Assess this cell for malaria.
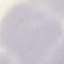
It is uninfected.

Summary:
  - Stain: Giemsa
  - Preparation: thin smear
  - Capture: smartphone camera at the microscope eyepiece
  - Image type: cell patch, automatically extracted from a larger field of view and resized to 64 × 64 pixels